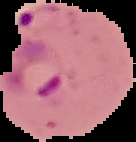

Image is 136×142 pixels. From a thin blood smear. Malaria status: parasitized. Segmented cell region on a black background.